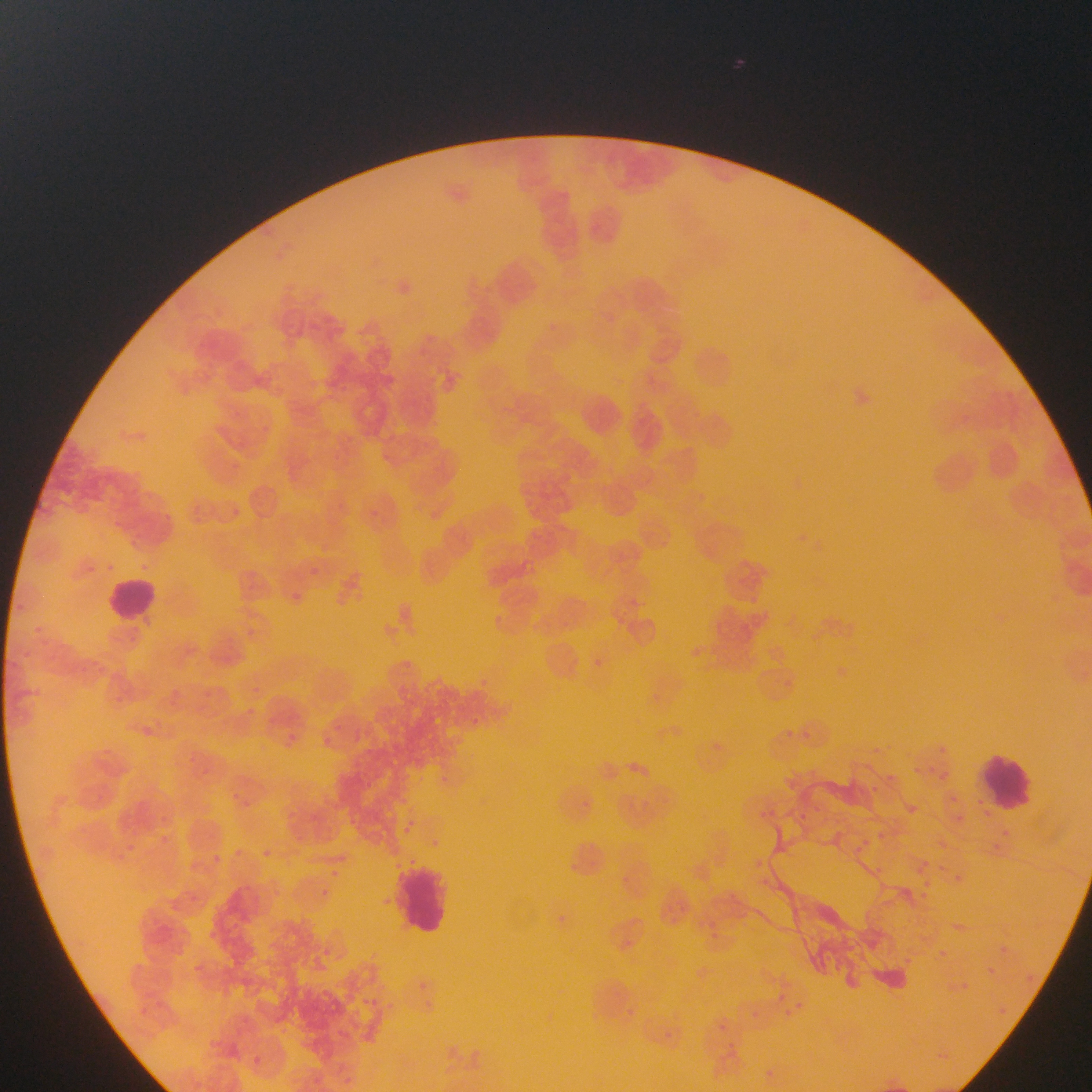

country: Ghana
plasmodium_parasite_locations: 'approximate bounding boxes as [left, top, right, bottom] in pixels: [139, 557, 151, 578], [103, 558, 114, 577], [303, 560, 322, 582], [86, 562, 94, 578], [289, 589, 308, 615], [338, 595, 354, 614], [14, 597, 24, 608], [489, 611, 506, 629], [33, 621, 48, 637], [243, 629, 255, 646], [20, 646, 31, 663], [591, 656, 603, 671], [473, 676, 513, 701], [248, 683, 264, 695], [168, 686, 193, 701], [250, 704, 259, 720], [467, 717, 484, 736], [133, 721, 159, 744], [787, 725, 800, 740], [348, 727, 364, 745], [802, 727, 812, 746], [285, 732, 293, 743], [318, 733, 338, 749], [945, 734, 964, 754], [710, 738, 720, 746], [876, 746, 882, 756], [187, 752, 199, 764], [929, 762, 941, 781], [202, 763, 214, 773], [882, 768, 901, 787], [945, 768, 960, 786], [436, 773, 456, 794], [229, 791, 239, 802], [951, 792, 965, 808], [239, 796, 250, 808], [578, 798, 594, 817], [907, 805, 921, 820], [771, 806, 783, 824], [800, 809, 808, 822], [160, 812, 174, 829], [401, 818, 423, 842], [159, 833, 169, 843], [121, 835, 142, 856], [853, 835, 868, 856], [864, 840, 876, 845], [992, 842, 1019, 867], [228, 843, 240, 855], [259, 844, 274, 858], [114, 847, 127, 866], [214, 848, 222, 864], [750, 848, 765, 872], [875, 856, 894, 876], [925, 859, 935, 868], [940, 862, 955, 879], [331, 865, 344, 877], [949, 871, 966, 887], [625, 873, 643, 894], [318, 883, 328, 896], [924, 890, 945, 906], [557, 907, 572, 929], [705, 918, 725, 936], [997, 942, 1006, 949], [983, 964, 998, 978], [956, 979, 972, 994], [769, 982, 801, 1007], [792, 997, 803, 1013], [618, 1001, 632, 1033], [753, 1006, 773, 1027], [787, 1010, 792, 1020], [715, 1015, 730, 1032], [657, 1023, 687, 1053], [726, 1038, 741, 1052], [758, 1063, 779, 1082] | approximate [x, y] pixel centers of objects too small to bound: [1005, 830]'
capture: mobile-phone photograph through a microscope
leukocyte_locations: 'approximate bounding boxes as [left, top, right, bottom] in pixels: [101, 576, 161, 628], [978, 752, 1040, 813], [396, 864, 455, 937]'
preparation: thin blood film
field_of_view: single
image_size: 1092×1092 pixels